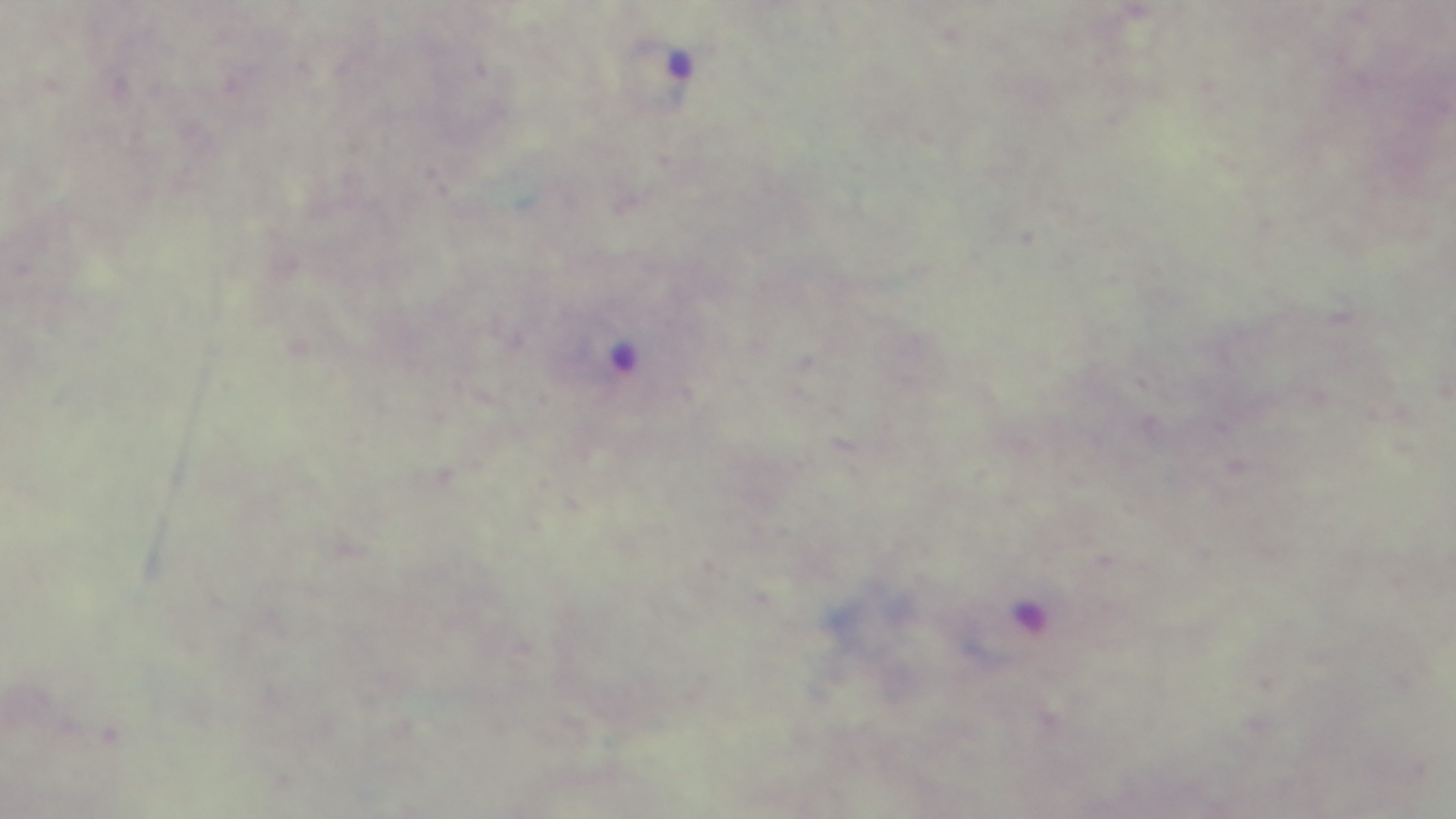

{
  "field_of_view": "single",
  "malaria_status": "positive",
  "capture": "mounted 4K digital camera",
  "preparation": "thick blood film",
  "stain": "Giemsa",
  "modality": "light microscopy",
  "objective": "100x oil immersion"
}